Name the blood parasite species.
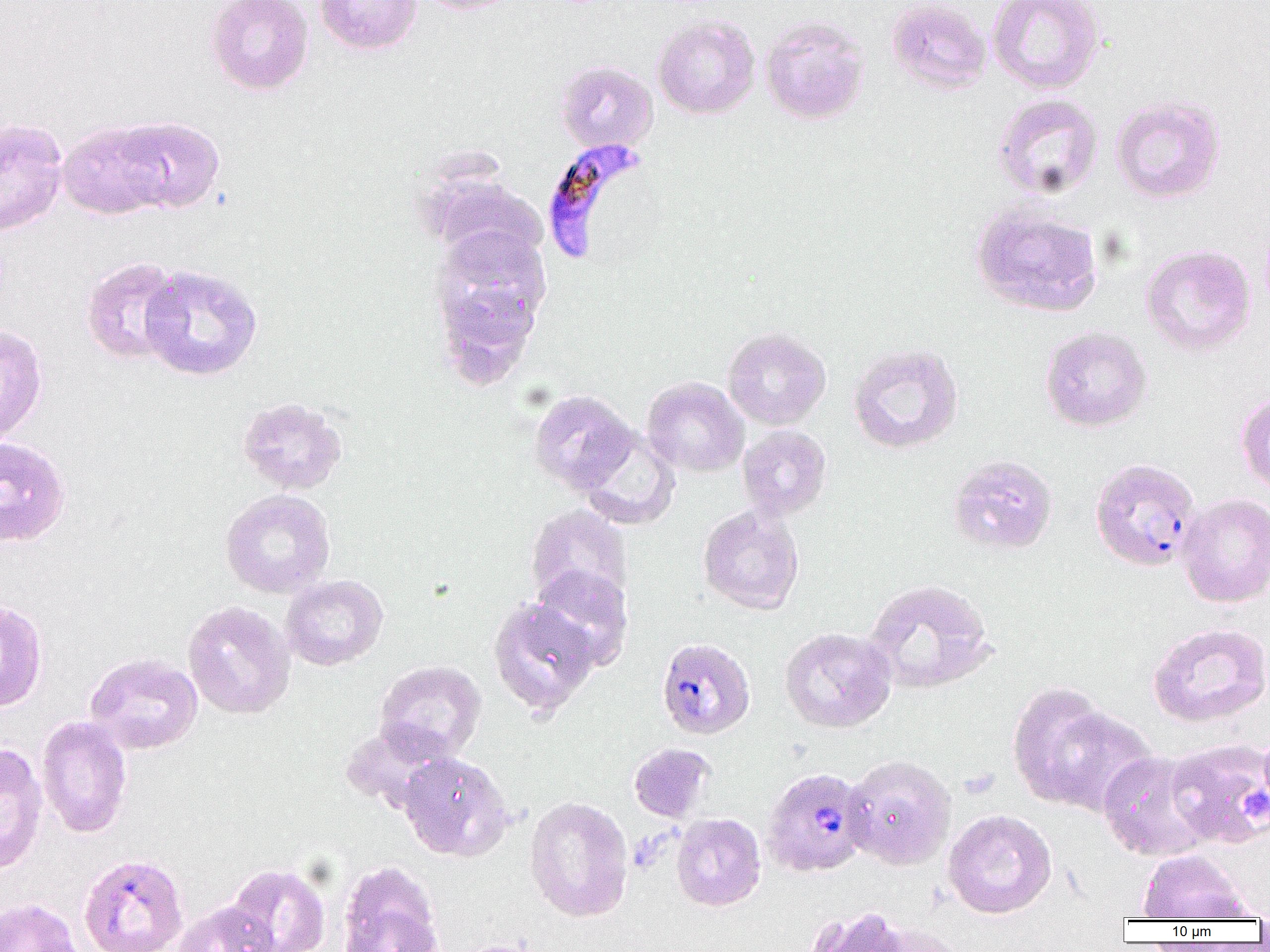
Plasmodium falciparum.

Approximate bounding boxes as (x1, y1, x2, y2) in pixels. Plasmodium falciparum-infected red blood cell locations: (540, 138, 650, 266), (1089, 457, 1200, 572), (656, 637, 756, 740), (762, 767, 872, 878). Uninfected red blood cell locations: (205, 0, 314, 95), (314, 0, 423, 55), (415, 0, 521, 15), (886, 0, 992, 94), (987, 0, 1105, 94), (652, 15, 760, 119), (760, 15, 870, 125), (554, 60, 658, 153), (992, 93, 1103, 200), (1110, 94, 1226, 204), (110, 116, 225, 214), (0, 118, 68, 236), (58, 121, 171, 220), (419, 171, 548, 266), (971, 205, 1103, 317), (430, 225, 551, 354), (1140, 244, 1256, 356), (80, 257, 183, 366), (138, 263, 263, 382), (0, 322, 48, 446), (1040, 326, 1152, 432), (723, 327, 831, 430), (847, 343, 964, 454), (641, 377, 748, 477), (529, 389, 637, 494), (1236, 391, 1270, 497), (236, 396, 348, 495), (737, 425, 832, 521), (576, 427, 681, 530), (0, 437, 72, 546), (947, 454, 1058, 555), (220, 489, 335, 598), (1178, 493, 1270, 608), (525, 504, 633, 612), (698, 505, 804, 615), (529, 565, 634, 670), (280, 574, 388, 671), (864, 577, 996, 695), (488, 598, 600, 716), (0, 599, 48, 712), (182, 600, 295, 720), (1147, 622, 1270, 727), (779, 627, 896, 733), (85, 652, 203, 754), (374, 659, 486, 764), (1008, 681, 1122, 810), (1040, 705, 1159, 818), (36, 715, 133, 839), (339, 723, 454, 815), (1165, 738, 1270, 849), (0, 743, 48, 875), (628, 743, 715, 822), (1097, 750, 1216, 862), (398, 751, 513, 861), (843, 754, 957, 870), (525, 795, 634, 922), (942, 809, 1057, 919), (671, 813, 766, 911), (1137, 849, 1253, 921), (78, 853, 189, 952), (337, 860, 444, 952), (223, 862, 331, 952), (0, 897, 83, 952), (171, 899, 280, 952), (805, 906, 920, 952), (866, 923, 974, 952), (444, 939, 548, 952). Platelet locations: (1240, 788, 1269, 823). Captured at 1000x magnification. Image is 1270×952 pixels. One field of a larger specimen. Thin blood film. Optical microscopy.